Report the malaria status of this cell.
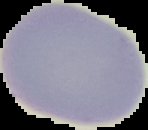

It is uninfected.

image size = 148×130 pixels
image type = segmented cell region on a black background
preparation = thin blood smear